Point out each Plasmodium parasite.
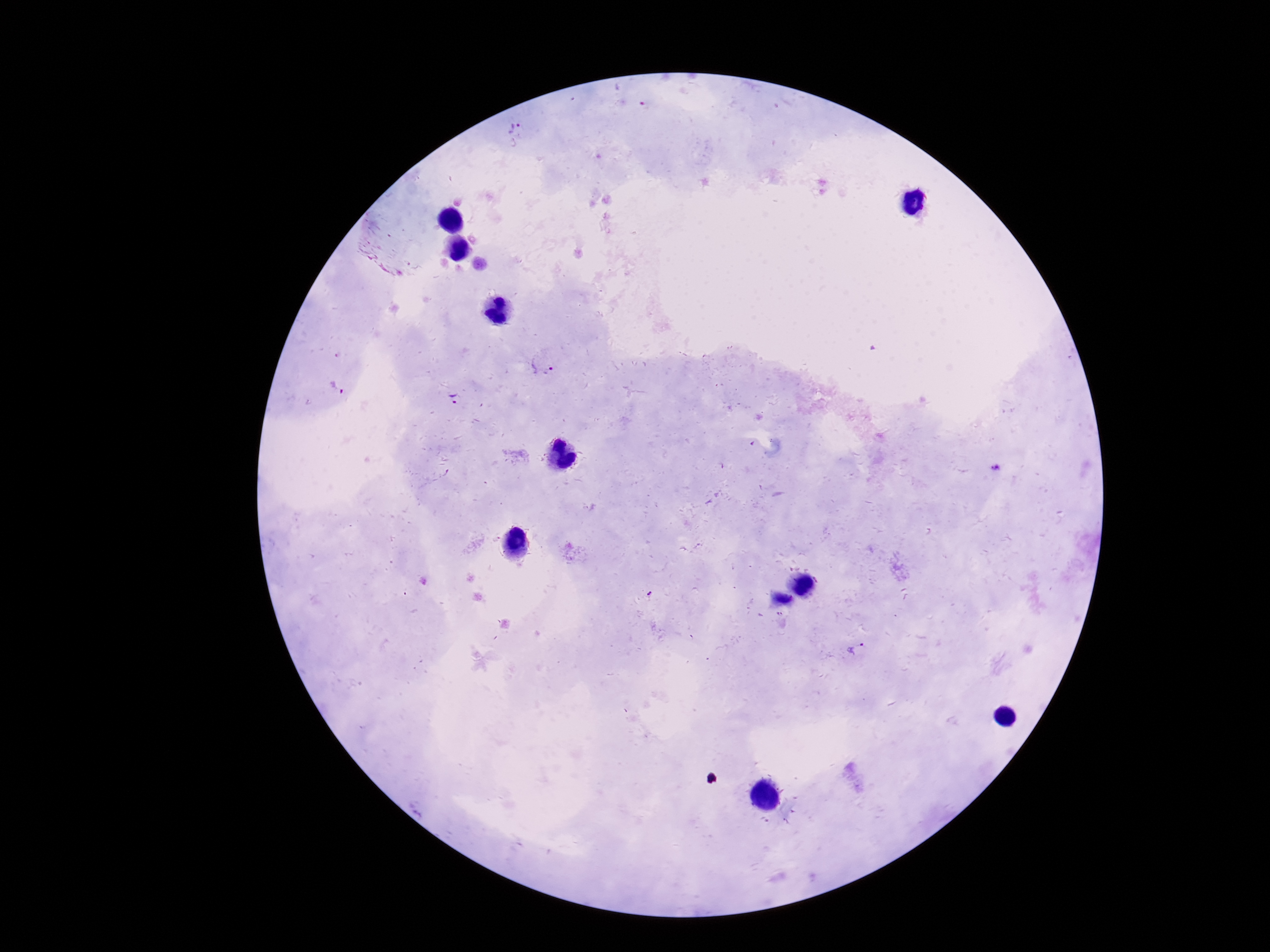

Approximate object centers, in pixels from the top-left corner.
Plasmodium parasites: (x=515, y=128), (x=542, y=368), (x=337, y=389), (x=453, y=399), (x=997, y=468), (x=780, y=615), (x=857, y=648).

{
  "field_of_view": "one from this slide",
  "capture": "smartphone camera through the microscope eyepiece",
  "preparation": "thick blood film",
  "patient_malaria_status": "positive",
  "image_size": "1270×952 pixels",
  "magnification": "100x",
  "stain": "Giemsa"
}